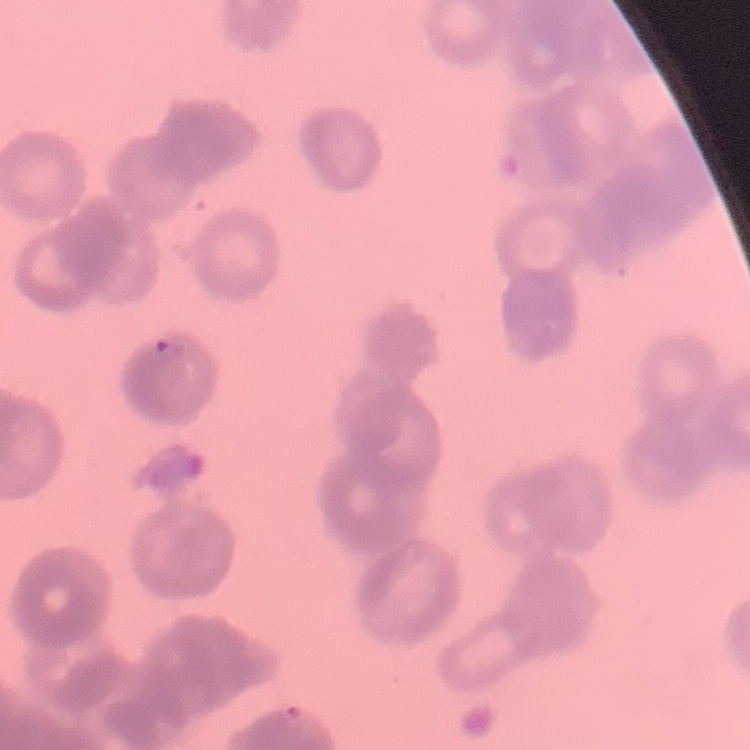
red_blood_cell_morphology: rouleaux formation
preparation: thin peripheral smear
stain: Field's or Giemsa
image_type: square crop of a larger photomicrograph